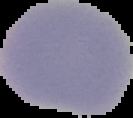
{
  "result": "negative for malaria parasites",
  "image_type": "segmented cell region on a black background",
  "preparation": "thin blood smear",
  "image_size": "133×118 pixels"
}